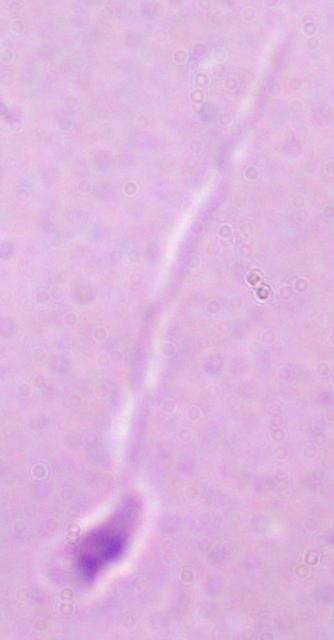
Summary:
  - Identification: Leishmania
  - Modality: photomicrograph
  - Magnification: 1000x